Locate every Plasmodium parasite.
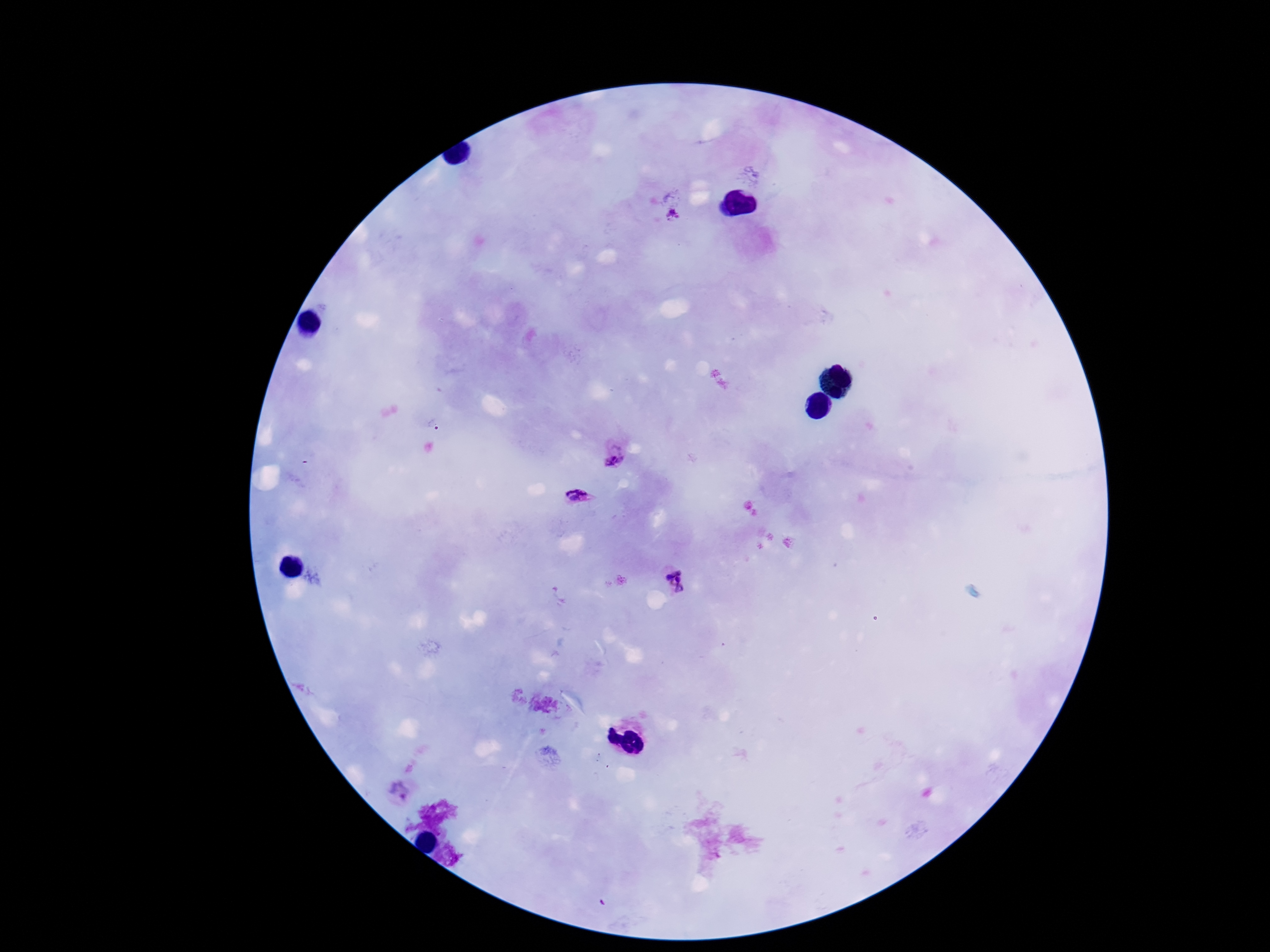
Approximate centers as {x, y} in pixels.
Plasmodium parasites: {672, 214}, {616, 457}, {580, 496}, {678, 583}, {401, 791}.

magnification = 100x
capture = smartphone camera through the microscope eyepiece
patient malaria status = positive
image size = 1270×952 pixels
field of view = single
stain = Giemsa
preparation = thick blood film